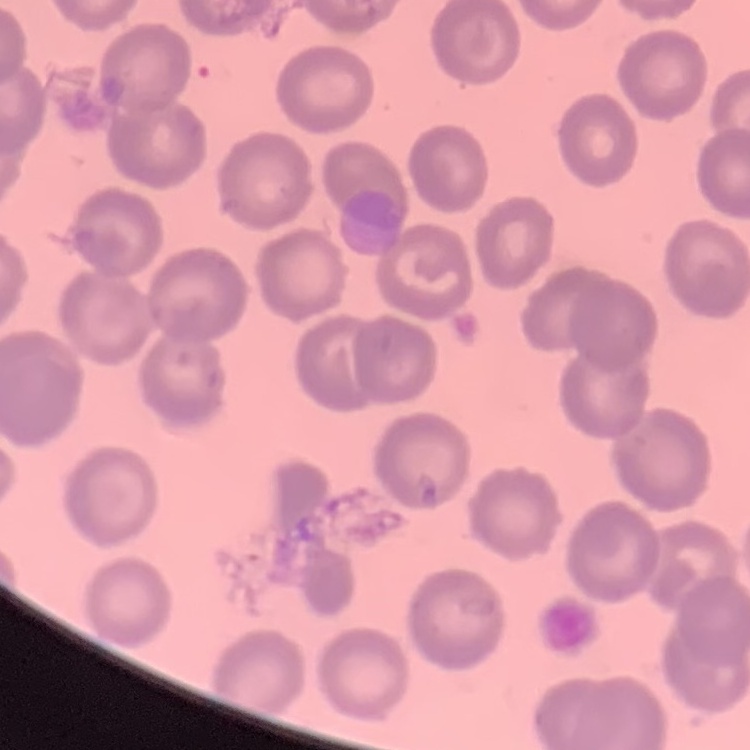
erythrocyte morphology = no rouleaux formation
stain = Field's or Giemsa
preparation = thin blood film
image type = square crop of a larger photomicrograph